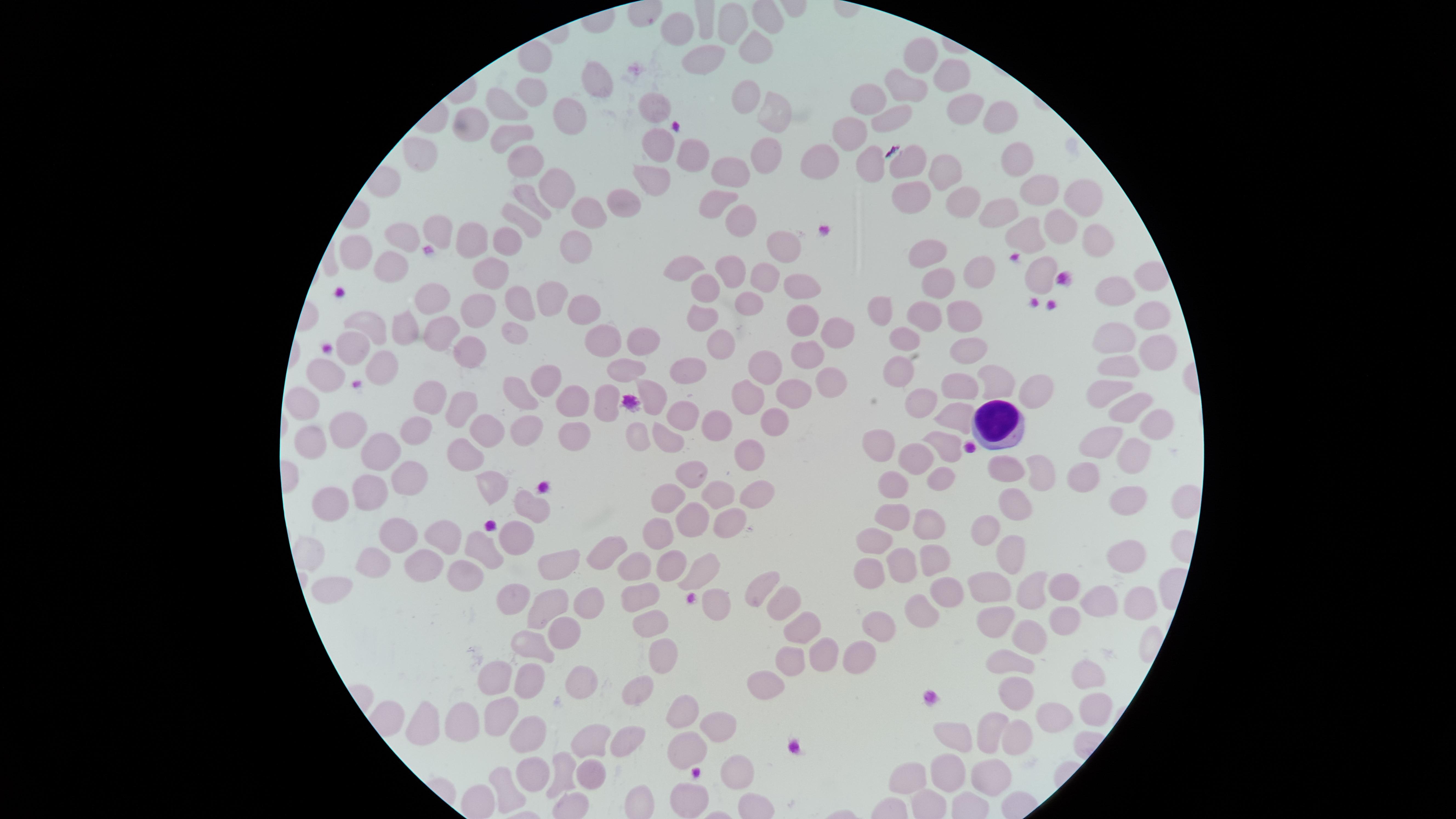 Approximate marker points, in pixels from the top-left corner. Uninfected RBCs: (x=734, y=21), (x=676, y=28), (x=756, y=50), (x=921, y=54), (x=707, y=59), (x=597, y=83), (x=954, y=84), (x=906, y=88), (x=532, y=91), (x=743, y=97), (x=869, y=98), (x=656, y=104), (x=508, y=108), (x=962, y=110), (x=772, y=118), (x=473, y=119), (x=998, y=119), (x=570, y=123), (x=888, y=123), (x=849, y=131), (x=510, y=134), (x=689, y=153), (x=419, y=155), (x=650, y=156), (x=524, y=159), (x=762, y=160), (x=1016, y=161), (x=877, y=162), (x=817, y=164), (x=910, y=165), (x=730, y=172), (x=948, y=173), (x=645, y=177), (x=552, y=179), (x=1042, y=189), (x=1084, y=195), (x=908, y=198), (x=521, y=201), (x=956, y=201), (x=625, y=203), (x=714, y=204), (x=998, y=209), (x=593, y=210), (x=735, y=218), (x=523, y=222), (x=1055, y=222), (x=1024, y=229), (x=402, y=237), (x=438, y=237), (x=1097, y=237), (x=465, y=239), (x=510, y=241), (x=784, y=244), (x=568, y=249), (x=360, y=252), (x=918, y=255), (x=688, y=264), (x=979, y=267), (x=729, y=268), (x=492, y=269), (x=389, y=271), (x=1042, y=271), (x=1143, y=277), (x=760, y=280), (x=932, y=283), (x=793, y=286), (x=550, y=293), (x=703, y=294), (x=438, y=298), (x=1111, y=298), (x=518, y=303), (x=745, y=304), (x=481, y=307), (x=584, y=309), (x=880, y=314), (x=922, y=318), (x=958, y=319), (x=1151, y=319), (x=796, y=322), (x=701, y=324), (x=368, y=325), (x=402, y=327), (x=514, y=330), (x=439, y=331), (x=829, y=336), (x=903, y=339), (x=1111, y=341), (x=635, y=342), (x=604, y=346), (x=714, y=346), (x=350, y=349), (x=957, y=349), (x=803, y=354), (x=1163, y=360), (x=468, y=362), (x=682, y=366), (x=763, y=366), (x=381, y=371), (x=1124, y=372), (x=624, y=374), (x=329, y=376), (x=825, y=376), (x=894, y=376), (x=997, y=377), (x=548, y=385), (x=957, y=385), (x=1108, y=387), (x=1026, y=390), (x=652, y=393), (x=786, y=394), (x=517, y=395), (x=427, y=399), (x=564, y=399), (x=302, y=402), (x=747, y=402), (x=914, y=402), (x=608, y=404), (x=1124, y=405), (x=458, y=414), (x=678, y=417), (x=1152, y=418), (x=956, y=419), (x=717, y=422), (x=772, y=427), (x=489, y=428), (x=408, y=429), (x=343, y=431), (x=575, y=431), (x=525, y=432), (x=635, y=435), (x=306, y=438), (x=1103, y=438), (x=668, y=442), (x=884, y=443), (x=384, y=451), (x=749, y=456), (x=921, y=456), (x=1135, y=456), (x=473, y=458), (x=691, y=469), (x=406, y=472), (x=1014, y=473), (x=1043, y=477), (x=937, y=481), (x=1085, y=481), (x=491, y=489), (x=752, y=493), (x=890, y=493), (x=366, y=496), (x=717, y=496), (x=668, y=498), (x=330, y=503), (x=1121, y=503), (x=1013, y=505), (x=1184, y=506), (x=528, y=508), (x=686, y=518), (x=893, y=520), (x=726, y=523), (x=927, y=526), (x=399, y=535), (x=660, y=536), (x=985, y=537), (x=509, y=538), (x=438, y=539), (x=484, y=542), (x=868, y=543), (x=614, y=548), (x=1124, y=555), (x=1006, y=557), (x=376, y=559), (x=670, y=560), (x=939, y=560), (x=429, y=561), (x=902, y=562), (x=556, y=563), (x=635, y=566), (x=869, y=573), (x=701, y=575), (x=458, y=579), (x=1072, y=582), (x=335, y=584), (x=991, y=585), (x=1036, y=587), (x=757, y=592), (x=513, y=594), (x=939, y=596), (x=643, y=598), (x=1097, y=599), (x=776, y=601), (x=1132, y=605), (x=548, y=606), (x=586, y=606), (x=713, y=606), (x=914, y=612), (x=997, y=614), (x=652, y=623), (x=880, y=623), (x=1060, y=624), (x=806, y=627), (x=564, y=632), (x=1023, y=637), (x=529, y=647), (x=823, y=652), (x=854, y=652), (x=661, y=654), (x=787, y=658), (x=1009, y=663), (x=502, y=676), (x=1088, y=676), (x=531, y=682), (x=578, y=682), (x=756, y=685), (x=640, y=687), (x=1006, y=692), (x=681, y=708), (x=1090, y=710), (x=498, y=716), (x=1048, y=718), (x=423, y=721), (x=462, y=722), (x=994, y=730), (x=531, y=732), (x=1014, y=732), (x=710, y=733), (x=632, y=736), (x=956, y=738), (x=593, y=741), (x=685, y=750), (x=560, y=768), (x=943, y=768), (x=735, y=771), (x=589, y=772), (x=984, y=772), (x=535, y=777), (x=912, y=778), (x=505, y=787), (x=692, y=799). WBCs: (x=999, y=422). The visible region is circular. Single field of view. Image is 1456×819 pixels. Photographed with a smartphone camera through the microscope eyepiece. Giemsa stain. Presence: no malaria parasites detected. Thin blood smear.